State the blood parasite species.
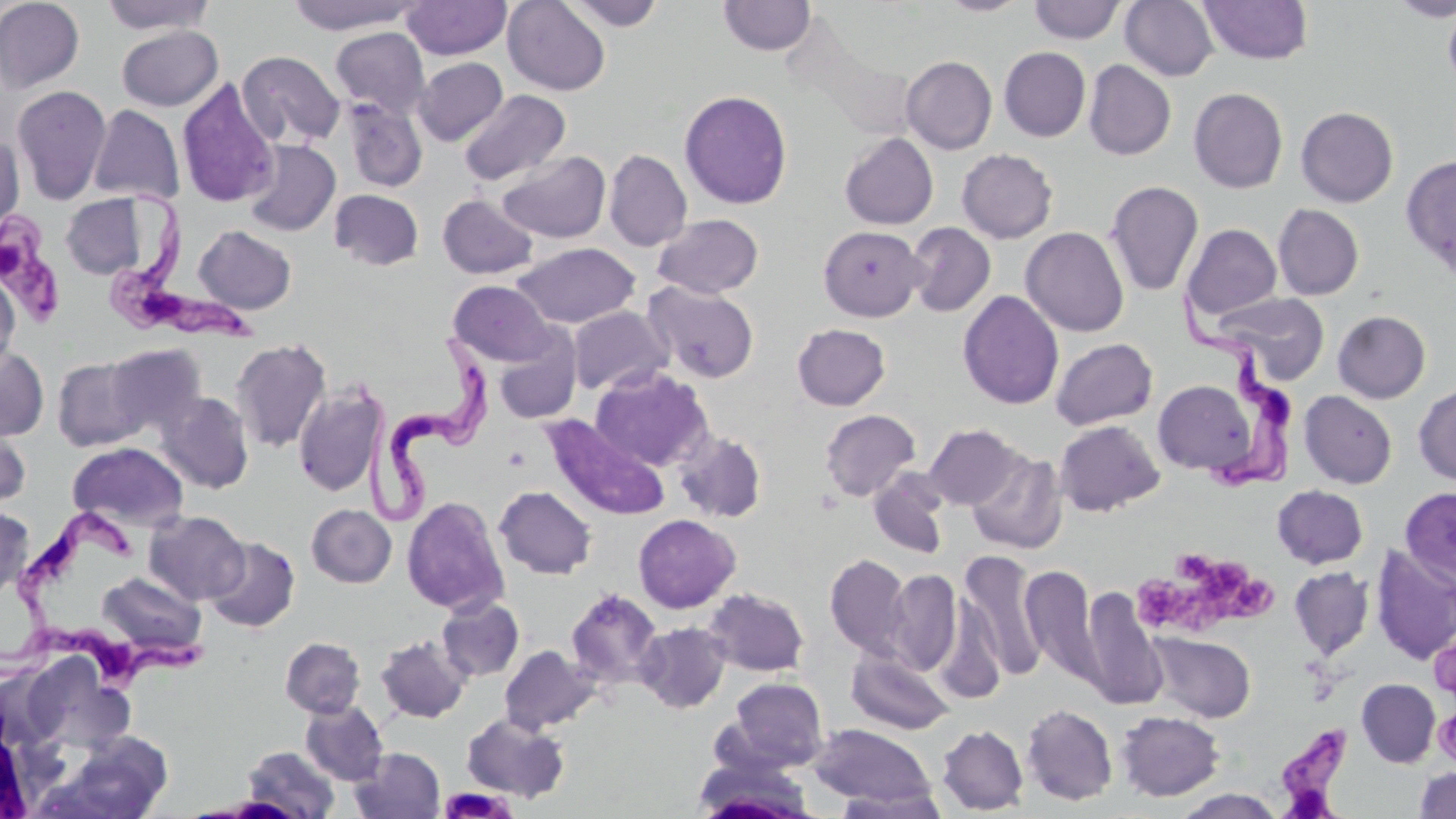

Trypanosoma brucei.

{
  "magnification": "1000x",
  "image_size": "1456×819 pixels",
  "modality": "light microscopy",
  "uninfected_red_blood_cell_locations": "approximate bounding boxes as (x1, y1, x2, y2) in pixels: (0, 0, 84, 93), (99, 0, 217, 35), (287, 0, 420, 34), (502, 0, 611, 95), (563, 0, 666, 31), (939, 0, 1029, 16), (1120, 0, 1219, 81), (1199, 0, 1314, 65), (1389, 0, 1456, 21), (402, 1, 511, 60), (719, 1, 816, 56), (1028, 1, 1126, 44), (1441, 5, 1456, 94), (116, 26, 222, 111), (330, 27, 430, 120), (998, 47, 1091, 141), (237, 50, 345, 149), (900, 56, 997, 154), (413, 57, 507, 146), (1083, 60, 1176, 160), (177, 77, 279, 208), (12, 84, 111, 205), (1188, 88, 1288, 193), (459, 89, 571, 186), (679, 89, 793, 209), (344, 98, 427, 193), (88, 104, 184, 204), (1295, 106, 1398, 207), (0, 131, 25, 238), (839, 133, 938, 230), (244, 140, 340, 236), (957, 148, 1058, 243), (604, 149, 692, 252), (497, 151, 611, 244), (1400, 154, 1456, 279), (1105, 181, 1204, 297), (329, 189, 423, 270), (61, 193, 150, 279), (437, 194, 538, 279), (1272, 204, 1364, 300), (653, 213, 764, 298), (906, 222, 996, 317), (1182, 223, 1282, 321), (193, 225, 296, 314), (818, 225, 926, 322), (1020, 226, 1130, 337), (512, 243, 640, 328), (0, 272, 20, 375), (448, 280, 558, 367), (644, 282, 759, 383), (957, 289, 1064, 409), (1213, 292, 1330, 383), (567, 306, 672, 395), (1332, 310, 1431, 403), (792, 323, 890, 410), (494, 331, 582, 424), (1050, 337, 1158, 430), (231, 338, 331, 453), (106, 343, 207, 437), (0, 346, 49, 440), (52, 357, 146, 451), (590, 366, 712, 471), (1153, 380, 1257, 475), (293, 383, 388, 497), (1414, 383, 1456, 486), (1299, 390, 1397, 489), (157, 391, 254, 494), (819, 409, 920, 502), (540, 417, 667, 521), (0, 420, 32, 509), (1054, 420, 1165, 516), (922, 423, 1023, 510), (674, 428, 768, 524), (67, 442, 188, 532), (967, 451, 1067, 555), (869, 471, 950, 559), (1272, 485, 1368, 569), (494, 486, 597, 579), (1400, 487, 1456, 587), (402, 496, 509, 616), (307, 504, 396, 587), (0, 505, 34, 600), (145, 511, 249, 605), (633, 514, 740, 613), (204, 536, 300, 633), (1370, 546, 1456, 665), (960, 551, 1047, 680), (824, 553, 912, 659), (1020, 564, 1101, 685), (1288, 566, 1374, 660), (885, 569, 962, 675), (97, 571, 206, 661), (704, 587, 809, 676), (1080, 587, 1167, 710), (566, 589, 663, 689), (437, 596, 524, 681), (634, 621, 732, 713), (1148, 632, 1256, 722), (375, 635, 471, 723), (280, 636, 365, 718), (499, 644, 600, 735), (846, 649, 954, 735), (21, 654, 134, 755), (727, 677, 828, 771), (1357, 678, 1440, 767), (301, 701, 388, 785), (1021, 703, 1118, 806), (1116, 710, 1225, 801), (461, 713, 570, 802), (809, 724, 938, 810), (937, 724, 1028, 814), (241, 745, 340, 818), (350, 747, 445, 819), (691, 761, 818, 818), (1415, 767, 1456, 818), (834, 789, 948, 818), (1175, 789, 1286, 818)",
  "preparation": "thin blood film",
  "trypanosoma_brucei_locations": "approximate bounding boxes as (x1, y1, x2, y2) in pixels: (103, 183, 267, 348), (0, 210, 63, 329), (1168, 292, 1297, 497), (358, 334, 495, 523), (8, 505, 140, 638), (0, 587, 211, 698), (1272, 723, 1357, 815)",
  "stain": "May-Grünwald-Giemsa",
  "platelet_locations": "approximate bounding boxes as (x1, y1, x2, y2) in pixels: (1172, 554, 1254, 599), (1135, 571, 1228, 635), (1219, 576, 1282, 627), (1434, 707, 1456, 768), (439, 786, 515, 817)",
  "field_of_view": "one of a larger specimen"
}